Classify this cell by malaria status.
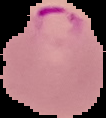

Parasitized.

Summary:
  - Image type: segmented cell region on a black background
  - Image size: 106×118 pixels
  - Preparation: thin blood smear